Classify this cell by malaria status.
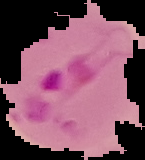
It is parasitized.

Summary:
  - Preparation: thin blood smear
  - Image size: 145×160 pixels
  - Image type: segmented cell region with the area outside set to black